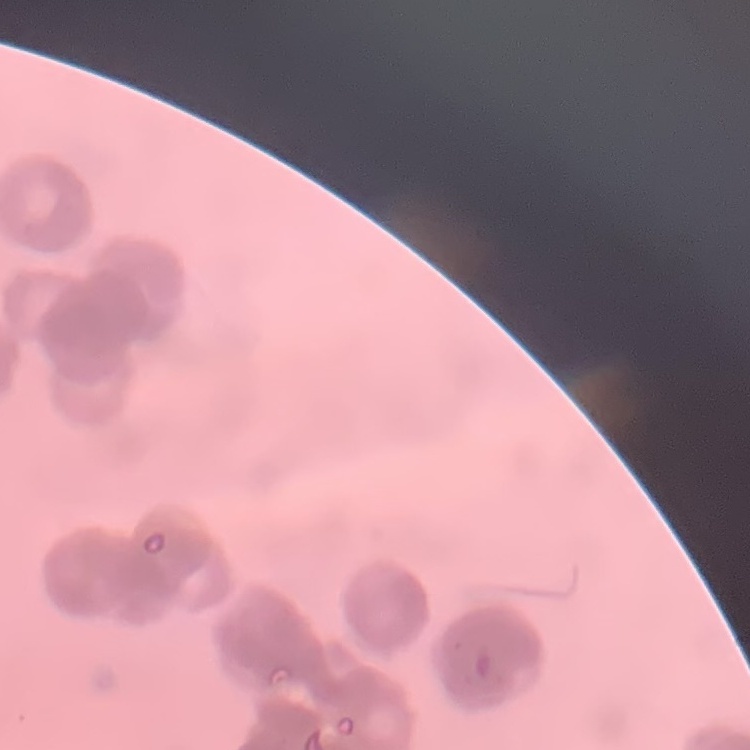
{
  "erythrocyte_morphology": "rouleaux formation",
  "preparation": "thin blood film",
  "stain": "Field's or Giemsa",
  "image_type": "one tile cut from a larger photomicrograph"
}